Report the malaria status of this cell.
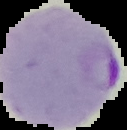
It is parasitized.

image type = segmented cell region with the area outside set to black
image size = 127×130 pixels
preparation = thin blood smear